Identify the cell.
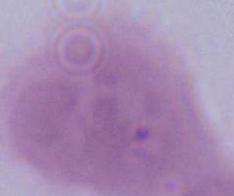

An erythrocyte.

1000x magnification. Photomicrograph.